Report the malaria status.
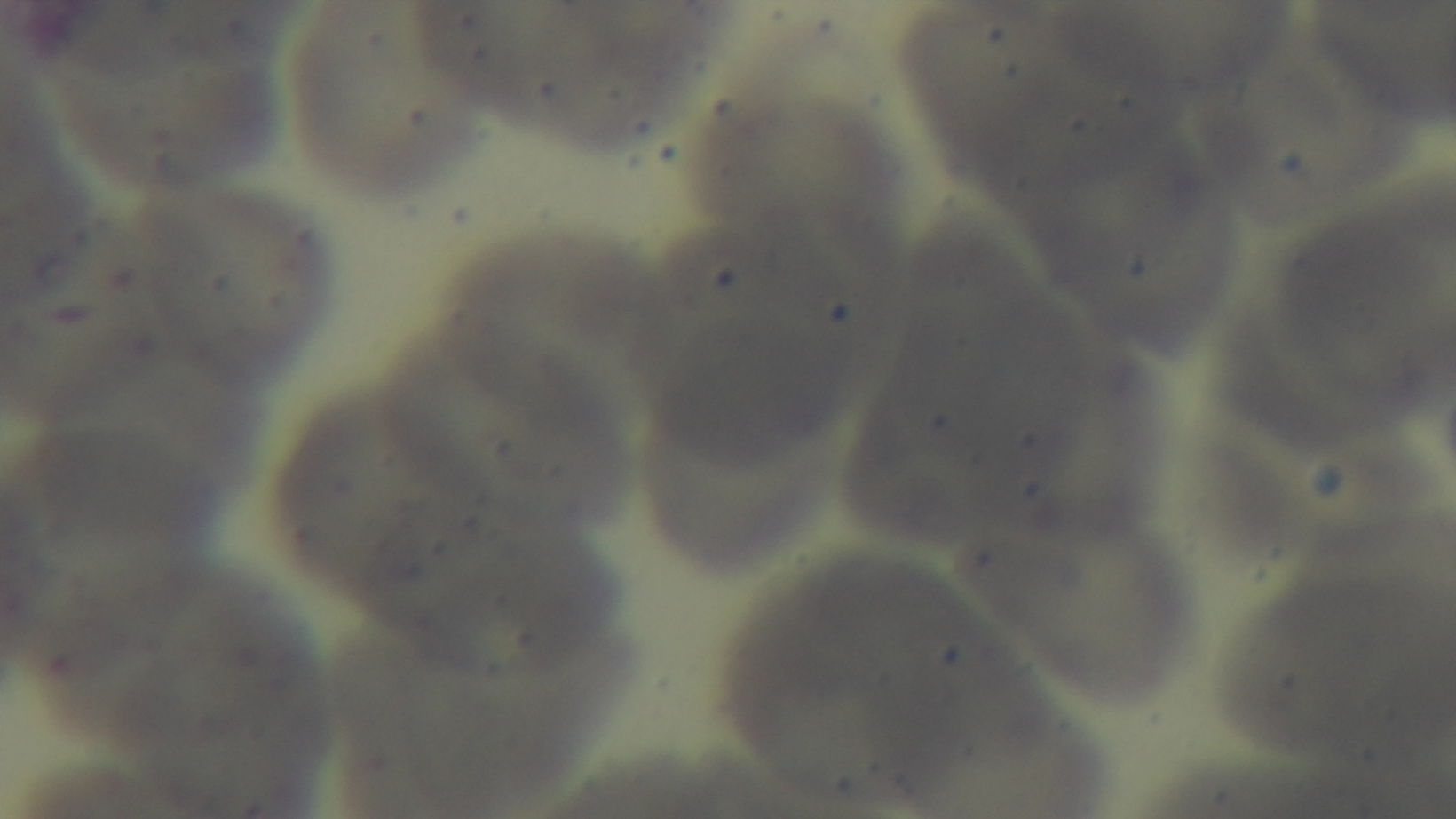
It is uninfected.

One field from the slide. Light microscopy. Mounted 4K digital camera. Preparation: thin smear. Giemsa-stained. 100x oil-immersion objective.